Locate every Plasmodium vivax-infected red blood cell.
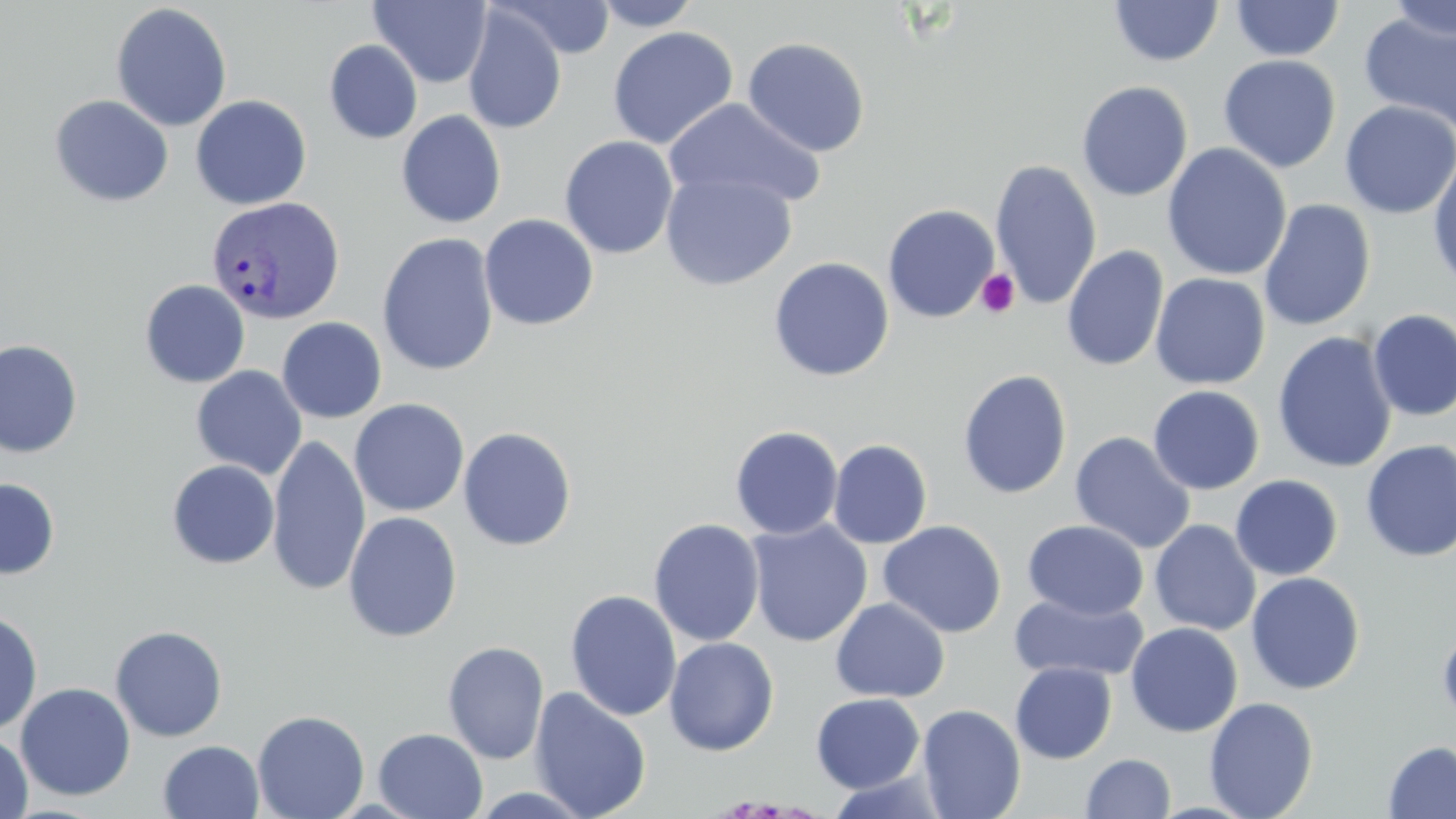

Approximate bounding boxes as (x1,y1)-(x2,y2) corner pairs in pixels.
Plasmodium vivax-infected red blood cells: (206,195)-(345,325).

Platelet locations: (974,268)-(1021,318). Uninfected red blood cell locations: (496,0)-(617,59), (592,0)-(703,31), (1230,0)-(1344,61), (1384,0)-(1456,42), (368,1)-(492,88), (1109,1)-(1224,67), (110,2)-(232,132), (461,6)-(567,135), (1359,10)-(1456,136), (607,26)-(739,149), (742,37)-(870,157), (324,40)-(423,144), (1217,55)-(1341,173), (1076,80)-(1193,202), (49,94)-(174,207), (191,95)-(312,210), (664,97)-(826,212), (1339,100)-(1456,218), (396,109)-(507,228), (559,135)-(678,259), (1162,142)-(1292,281), (1428,151)-(1456,292), (989,158)-(1102,310), (660,170)-(798,290), (1259,198)-(1376,332), (882,204)-(999,323), (479,213)-(599,331), (377,232)-(499,376), (1061,244)-(1169,372), (768,257)-(894,382), (1150,273)-(1271,391), (139,280)-(250,387), (1368,309)-(1456,421), (277,317)-(387,423), (1272,332)-(1397,474), (0,339)-(83,458), (191,365)-(307,479), (958,369)-(1073,499), (1148,385)-(1265,495), (350,398)-(469,517), (730,425)-(843,539), (458,426)-(577,551), (1069,432)-(1196,554), (267,435)-(370,595), (828,439)-(932,549), (1360,440)-(1456,562), (167,460)-(280,569), (1230,475)-(1343,580), (0,478)-(59,579), (343,511)-(463,642), (648,518)-(765,647), (746,519)-(873,647), (1021,519)-(1149,620), (1149,519)-(1261,636), (877,520)-(1008,638), (1246,571)-(1365,694), (565,589)-(682,722), (1009,593)-(1148,683), (830,598)-(950,703), (0,610)-(43,735), (1437,621)-(1456,731), (1125,622)-(1243,737), (109,625)-(228,742), (664,637)-(780,755), (442,641)-(549,764), (1010,661)-(1116,764), (15,682)-(136,801), (529,687)-(652,819), (811,692)-(925,794), (1204,697)-(1319,819), (916,703)-(1026,818), (252,709)-(370,819), (373,728)-(488,818), (0,731)-(33,818), (158,740)-(264,819), (1383,740)-(1456,819), (1081,753)-(1175,818). Slide-level diagnosis: Plasmodium vivax. Optical microscopy. Single field of view. 1000x magnification. May-Grünwald-Giemsa-stained preparation. Image is 1456×819 pixels. Thin blood film.